Give the extent of all uninfected red blood cells.
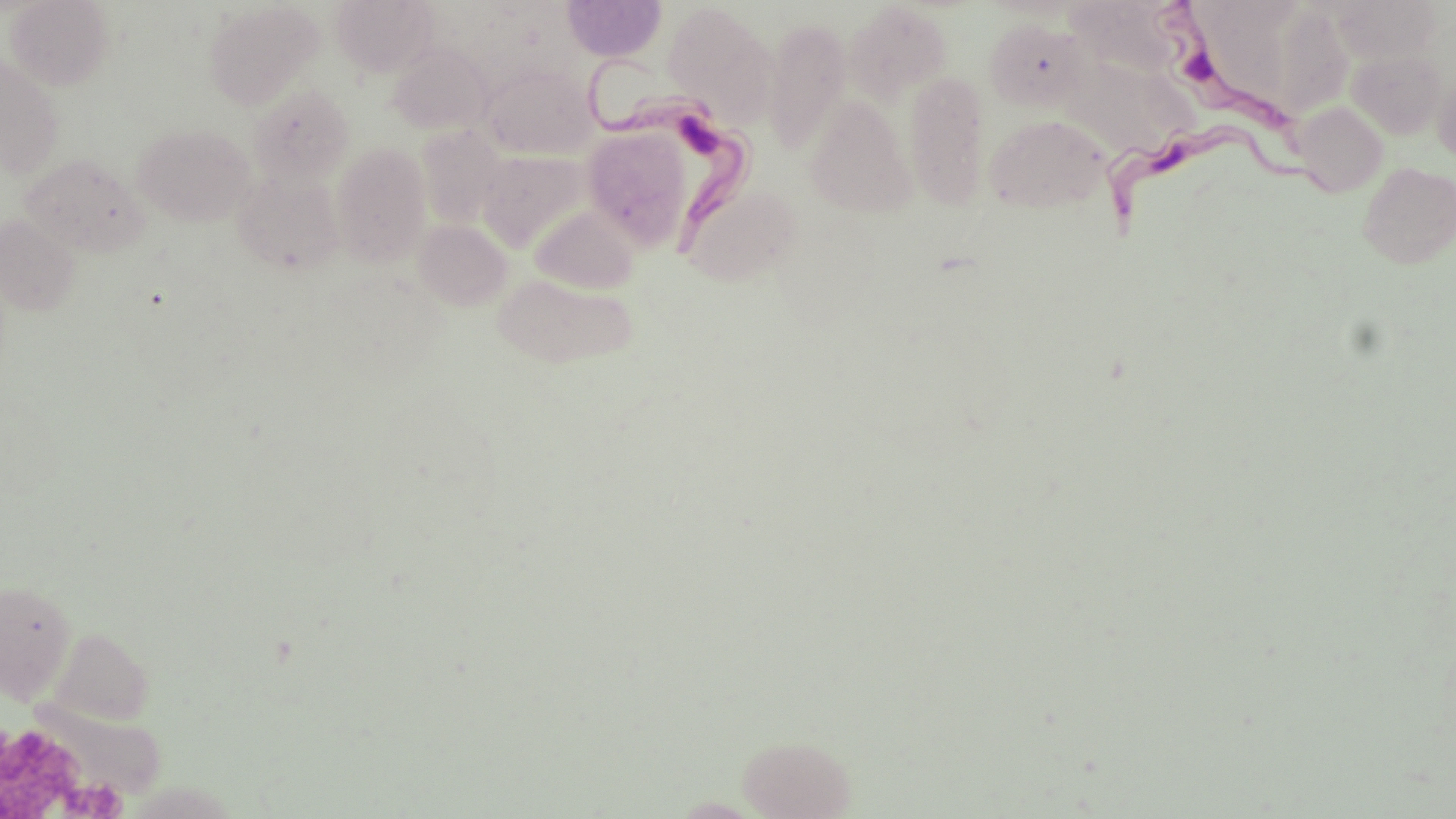
Approximate bounding boxes as (x1,y1)-(x2,y2) corner pairs in pixels.
Uninfected red blood cells: (5,0)-(114,91), (331,0)-(438,77), (561,0)-(667,62), (1063,0)-(1197,80), (1204,0)-(1295,96), (1275,0)-(1349,113), (1329,0)-(1441,63), (203,2)-(322,110), (661,3)-(777,124), (844,3)-(951,104), (763,16)-(852,157), (985,17)-(1093,112), (386,43)-(493,136), (1347,49)-(1448,139), (0,55)-(64,179), (1061,57)-(1193,158), (482,64)-(598,160), (904,69)-(991,212), (1432,72)-(1456,164), (249,84)-(354,186), (804,95)-(918,218), (1291,101)-(1388,197), (983,113)-(1112,213), (133,123)-(255,226), (580,124)-(699,252), (417,127)-(508,229), (330,141)-(432,266), (476,149)-(591,252), (19,153)-(149,259), (1358,161)-(1456,268), (233,171)-(345,274), (681,181)-(802,286), (530,205)-(640,294), (0,215)-(81,316), (414,219)-(512,310), (492,272)-(640,369), (0,579)-(76,703), (46,626)-(154,726), (35,703)-(168,801), (738,735)-(855,818).

{
  "slide_level_diagnosis": "Trypanosoma brucei",
  "preparation": "thin blood film",
  "modality": "optical microscopy",
  "trypanosoma_brucei_locations": "approximate bounding boxes as (x1,y1)-(x2,y2) corner pairs in pixels: (1145,0)-(1308,143), (583,57)-(756,258), (1099,118)-(1339,243)",
  "platelet_locations": "approximate bounding boxes as (x1,y1)-(x2,y2) corner pairs in pixels: (0,731)-(83,817), (60,776)-(130,817)",
  "magnification": "1000x",
  "field_of_view": "one of a larger specimen",
  "stain": "May-Grünwald-Giemsa",
  "image_size": "1456×819 pixels"
}